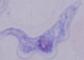

Summary:
  - Identification: trypanosome
  - Magnification: 1000x
  - Modality: photomicrograph